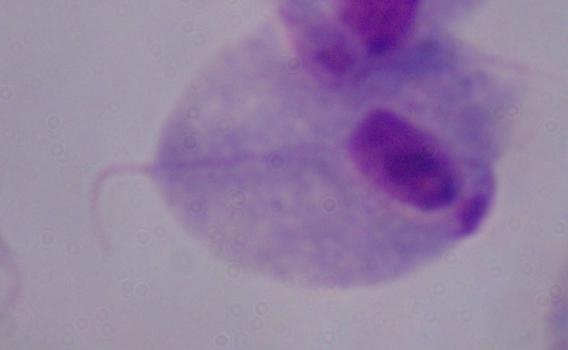

identification = trichomonad
magnification = 1000x
modality = photomicrograph